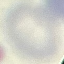

malaria_status: uninfected
capture: smartphone camera at the microscope eyepiece
stain: Giemsa
preparation: thin blood film
image_type: automatically extracted cell patch, resized to 64 × 64 pixels